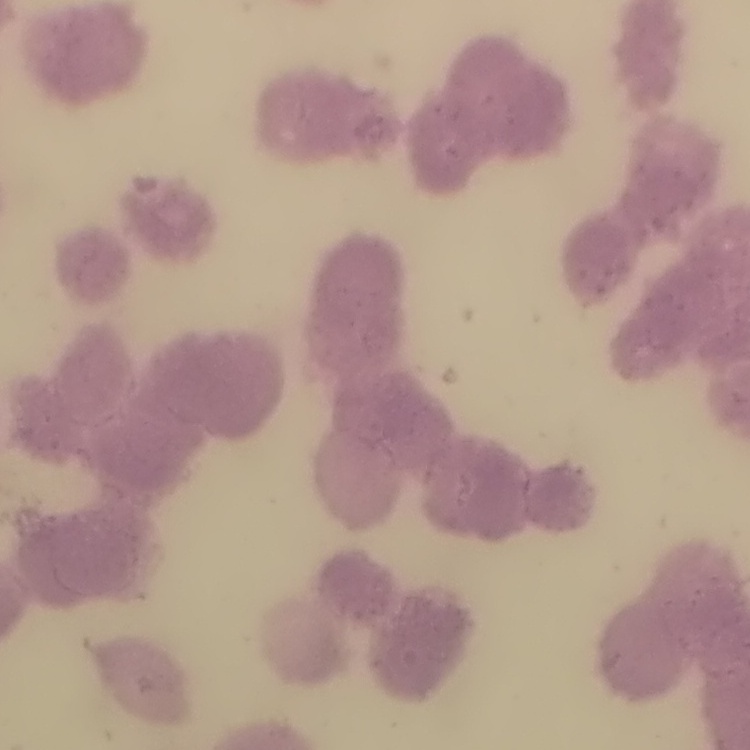

erythrocyte morphology = rouleaux formation
image type = one tile cut from a larger photomicrograph
stain = Field's or Giemsa
preparation = thin peripheral smear